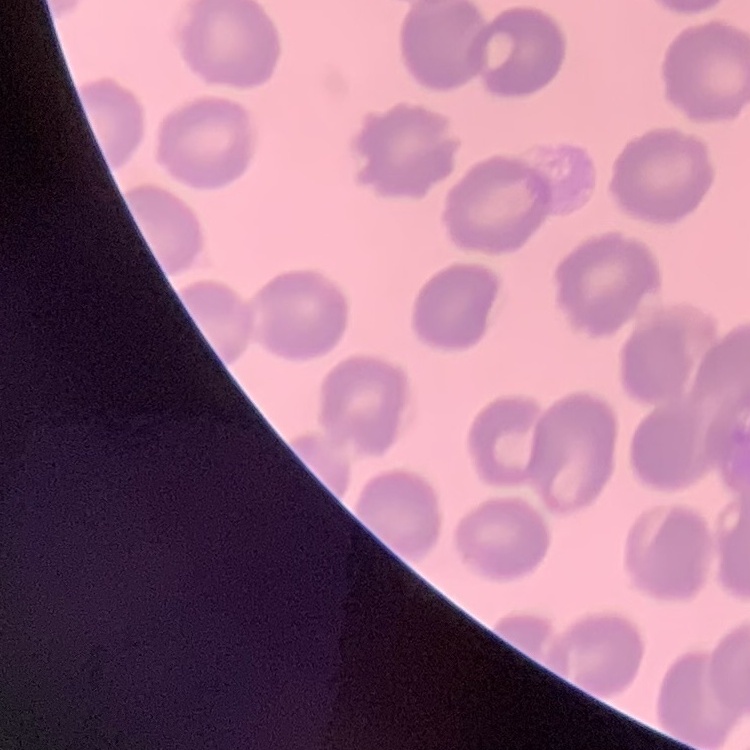
Summary:
  - Red blood cell morphology: no rouleaux formation
  - Image type: one tile cut from a larger photomicrograph
  - Stain: Field's or Giemsa
  - Preparation: thin peripheral smear